Name the parasite shown.
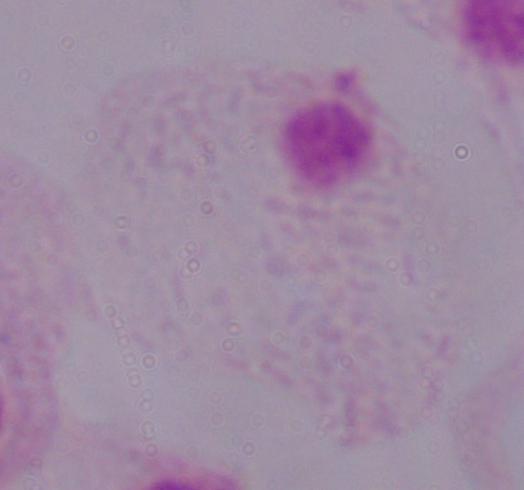

This is a trichomonad.

1000x magnification. Photomicrograph.